State which cell type is depicted.
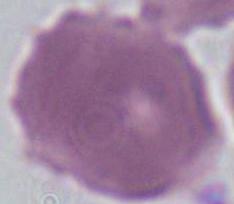

This is an erythrocyte.

Micrograph. 1000x magnification.